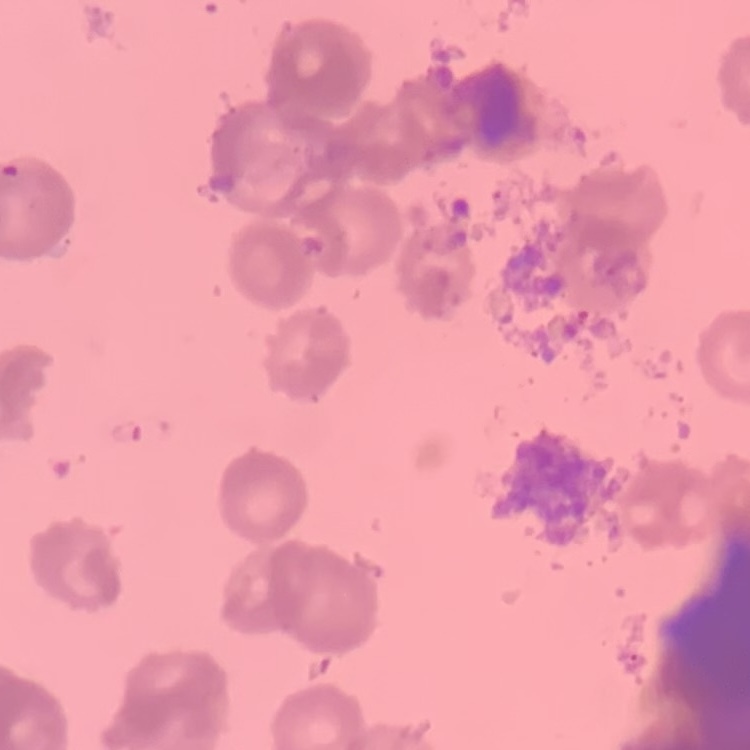
Summary:
  - Red blood cell morphology: rouleaux formation
  - Stain: Field's or Giemsa
  - Image type: square crop of a larger photomicrograph
  - Preparation: thin peripheral smear